Classify this cell by malaria status.
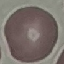

Uninfected.

Summary:
  - Stain: Giemsa
  - Capture: smartphone through the microscope eyepiece
  - Image type: cell patch, automatically extracted from a larger field of view and resized to 64 × 64 pixels
  - Preparation: thin blood smear